Locate every uninfected red blood cell.
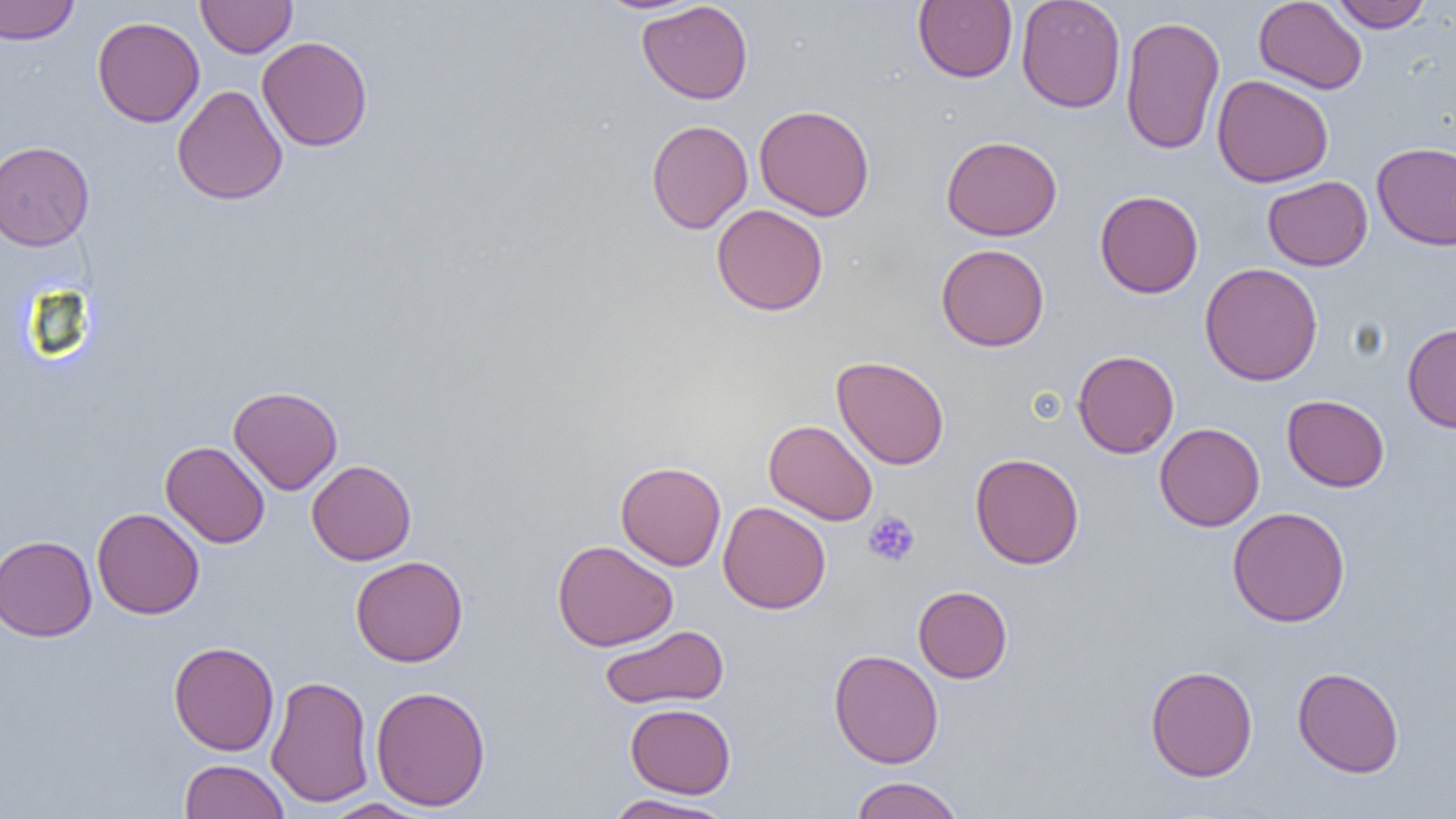
Approximate bounding boxes as [x1, y1, x2, y2] in pixels.
Uninfected red blood cells: [0, 0, 79, 45], [196, 0, 297, 58], [1016, 0, 1126, 113], [1253, 0, 1367, 94], [1329, 0, 1432, 32], [637, 1, 753, 104], [913, 1, 1017, 83], [1120, 15, 1225, 155], [92, 16, 205, 127], [257, 35, 373, 151], [1212, 74, 1333, 188], [172, 84, 287, 206], [754, 104, 875, 221], [646, 119, 753, 234], [941, 135, 1062, 241], [0, 140, 94, 251], [1371, 141, 1456, 251], [1262, 175, 1373, 271], [1094, 189, 1203, 298], [712, 204, 828, 316], [936, 243, 1049, 351], [1200, 262, 1323, 386], [1402, 323, 1456, 433], [1072, 350, 1179, 458], [831, 355, 950, 470], [228, 386, 343, 495], [1282, 395, 1390, 492], [764, 419, 878, 526], [1155, 423, 1265, 531], [161, 441, 270, 548], [970, 453, 1085, 569], [306, 460, 416, 565], [615, 461, 726, 570], [718, 501, 831, 614], [91, 507, 205, 619], [1227, 507, 1350, 626], [0, 534, 97, 642], [552, 540, 678, 652], [350, 555, 468, 666], [913, 585, 1012, 683], [600, 624, 728, 709], [168, 641, 279, 756], [828, 649, 943, 769], [1144, 664, 1258, 781], [1292, 666, 1404, 778], [265, 674, 375, 808], [370, 685, 491, 811], [625, 703, 736, 798], [179, 759, 289, 819], [849, 776, 965, 819], [602, 794, 734, 818], [320, 798, 431, 818].

{
  "slide_level_diagnosis": "negative for blood parasites",
  "field_of_view": "single",
  "magnification": "1000x",
  "image_size": "1456×819 pixels",
  "modality": "light microscopy",
  "platelet_locations": "approximate bounding boxes as [x1, y1, x2, y2] in pixels: [864, 510, 920, 566]",
  "preparation": "thin blood film"
}